State which cell type is depicted.
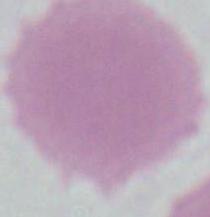
An erythrocyte.

magnification = 1000x
modality = micrograph